Name the blood parasite species.
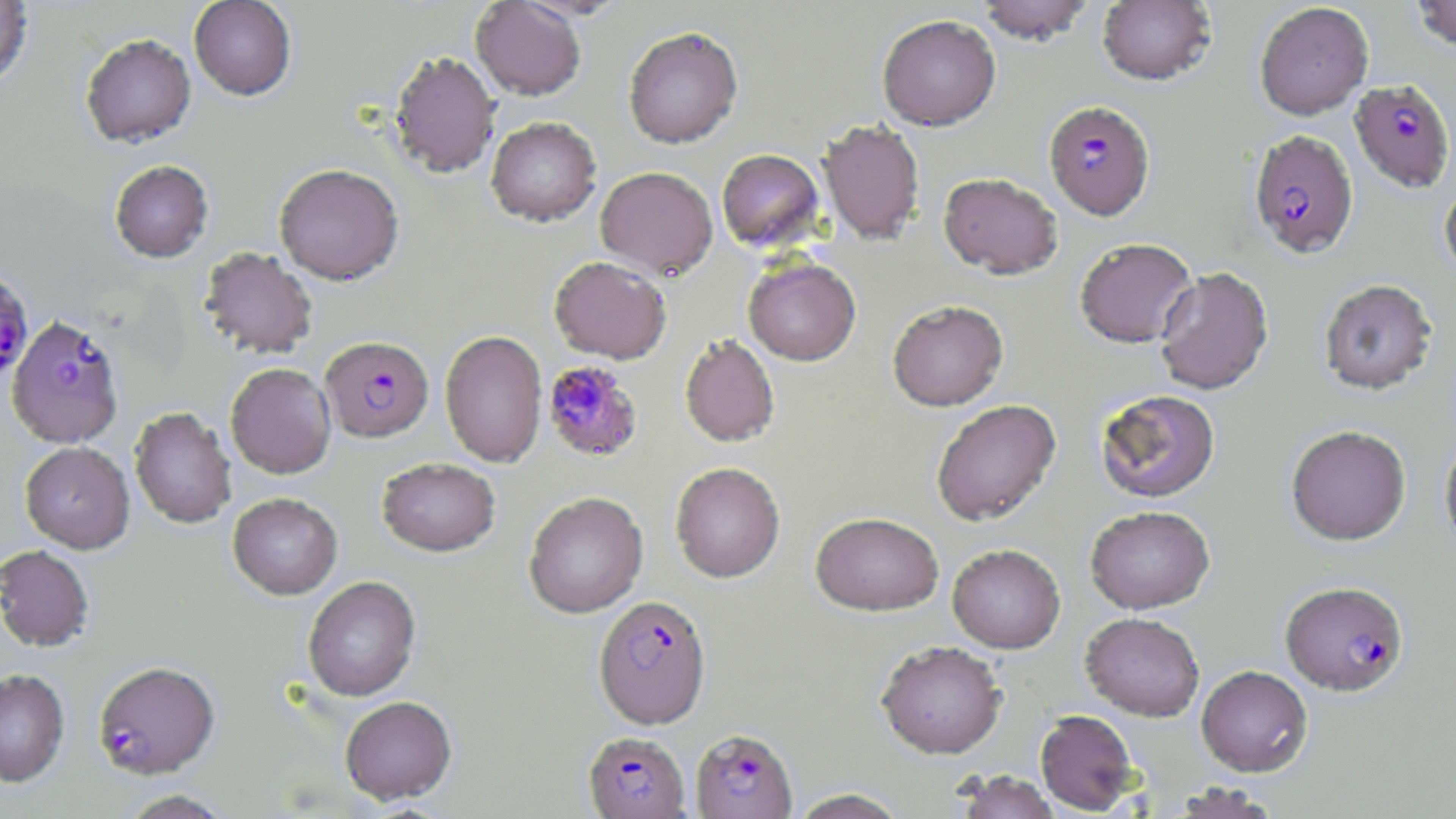

Plasmodium falciparum.

Approximate bounding boxes as [x1, y1, x2, y2] in pixels. Plasmodium falciparum-infected red blood cell locations: [1349, 79, 1455, 192], [1044, 101, 1155, 220], [1248, 129, 1359, 259], [0, 269, 34, 384], [7, 316, 124, 448], [321, 336, 434, 442], [542, 360, 643, 461], [1280, 581, 1409, 696], [594, 594, 711, 728], [93, 661, 219, 780], [690, 728, 798, 818], [583, 732, 690, 818]. Uninfected red blood cell locations: [0, 0, 34, 88], [189, 0, 296, 100], [975, 0, 1095, 45], [1097, 0, 1216, 86], [1411, 0, 1456, 52], [470, 1, 586, 100], [1255, 2, 1374, 120], [877, 15, 1001, 130], [623, 26, 743, 149], [80, 33, 196, 148], [389, 50, 501, 179], [485, 117, 601, 227], [819, 120, 925, 244], [716, 149, 825, 252], [109, 160, 214, 263], [274, 164, 404, 285], [595, 166, 718, 279], [938, 172, 1063, 279], [1440, 181, 1456, 283], [1074, 238, 1197, 349], [199, 247, 318, 359], [549, 256, 671, 363], [743, 258, 861, 366], [1154, 266, 1273, 395], [1318, 278, 1438, 395], [887, 300, 1009, 411], [440, 330, 547, 467], [679, 334, 780, 447], [226, 363, 336, 479], [1095, 389, 1221, 504], [931, 399, 1061, 526], [130, 407, 237, 529], [1286, 425, 1411, 545], [1439, 436, 1456, 554], [20, 442, 135, 553], [377, 457, 500, 557], [670, 462, 785, 583], [524, 491, 648, 618], [228, 493, 342, 599], [1085, 506, 1216, 614], [810, 511, 944, 616], [947, 544, 1065, 653], [0, 545, 94, 653], [302, 576, 420, 702], [1080, 612, 1204, 722], [875, 641, 1007, 759], [1196, 665, 1313, 777], [0, 669, 70, 787], [340, 696, 456, 805], [1035, 709, 1140, 814], [954, 770, 1060, 819], [1169, 782, 1284, 818], [789, 789, 908, 818], [117, 790, 234, 818]. Single field of view. Optical microscopy. 1000x magnification. Thin blood smear. Image is 1456×819 pixels. May-Grünwald-Giemsa stain.